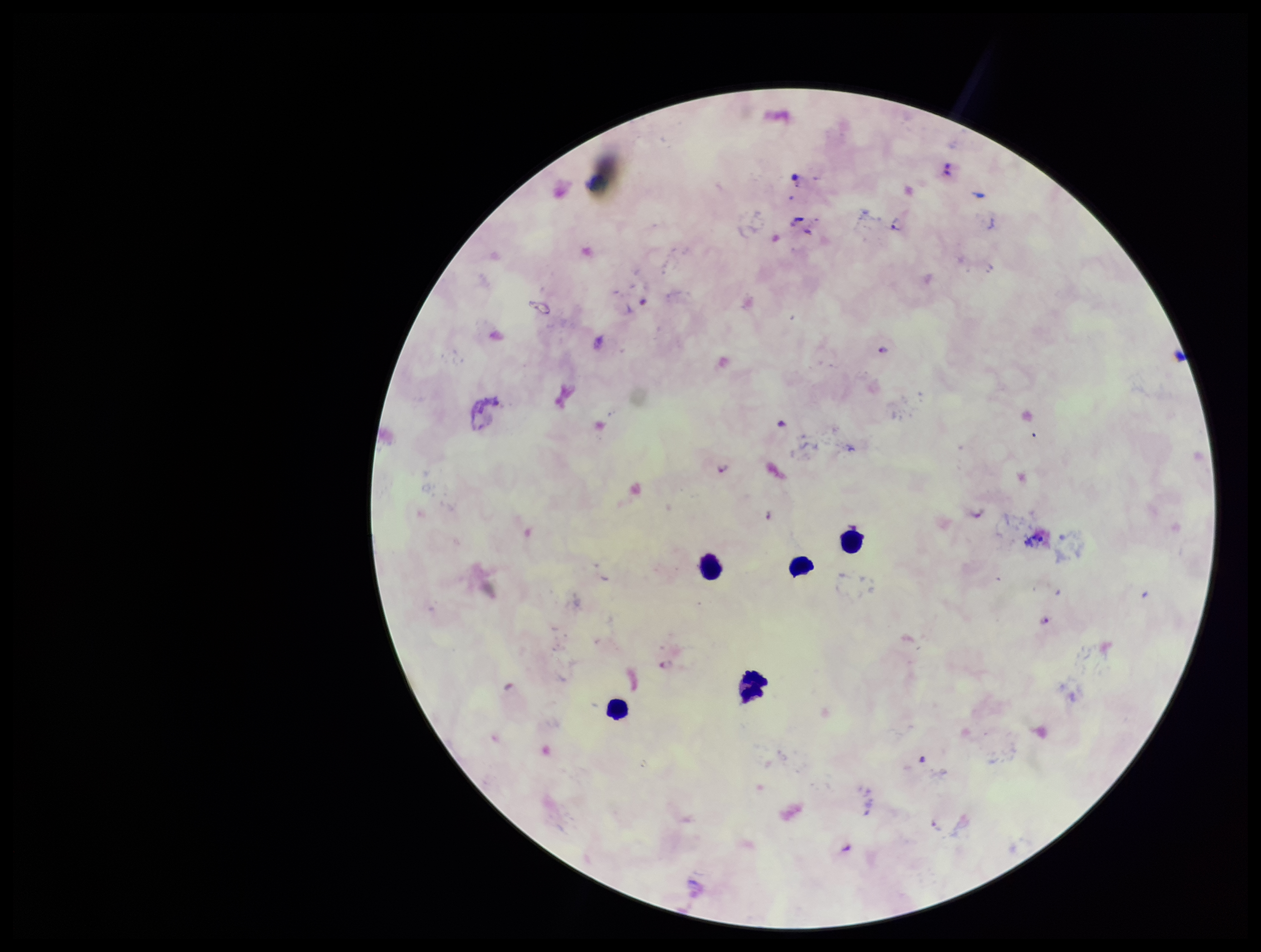
Summary:
  - Stain: Giemsa
  - Plasmodium parasites: seen
  - Field of view: single
  - Patient malaria status: positive
  - Capture: smartphone photograph through the microscope eyepiece
  - Species reported for this patient: Plasmodium falciparum
  - Parasite count: 5
  - Preparation: thick smear
  - Leukocyte count: 5
  - Image size: 1261×952 pixels